Identify the cell.
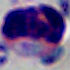
A leukocyte.

modality = micrograph
magnification = 1000x